Outline each uninfected red blood cell.
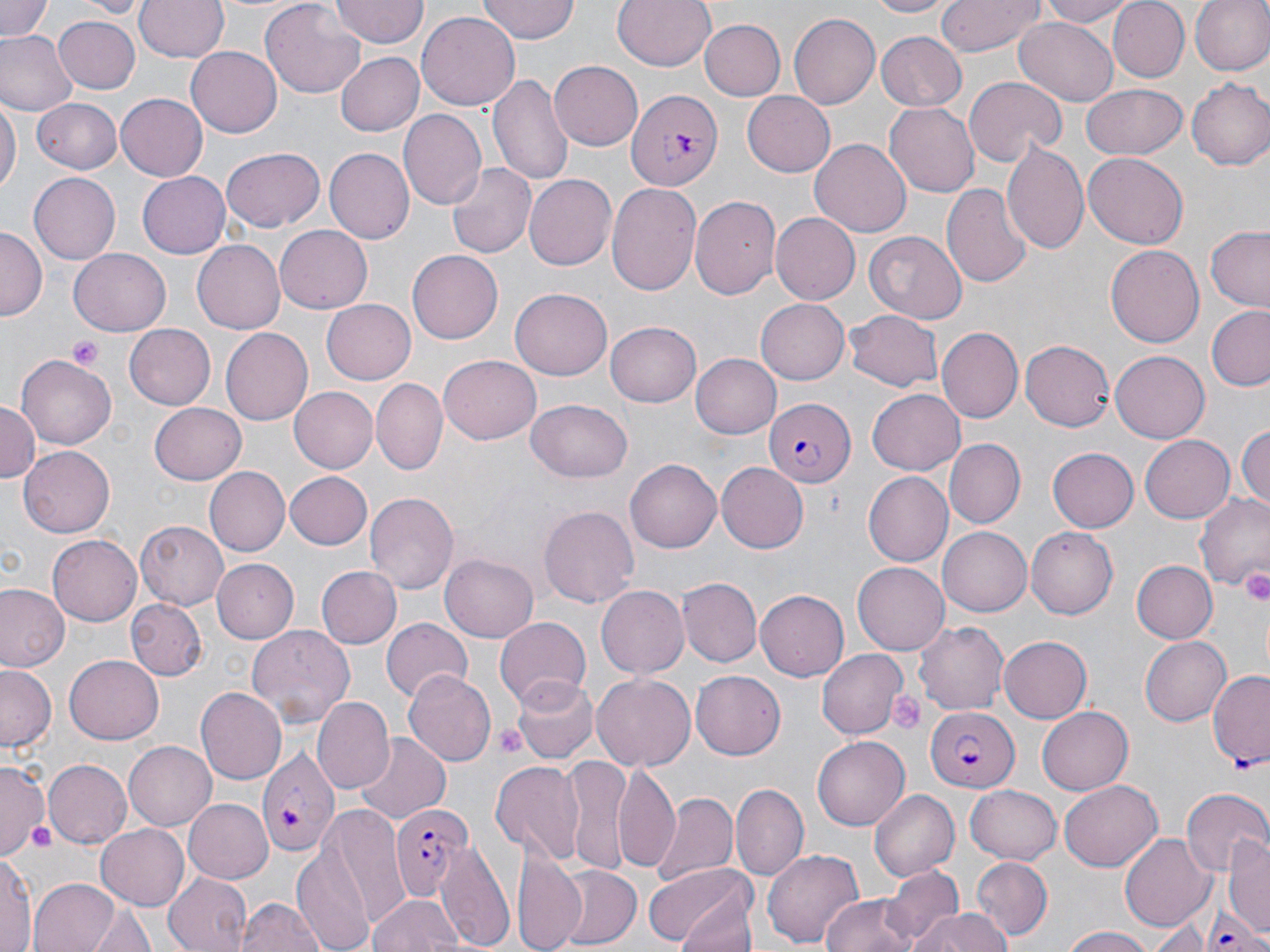
Approximate bounding boxes as (x1, y1, x2, y2) in pixels.
Uninfected red blood cells: (0, 0, 55, 42), (79, 0, 149, 18), (134, 0, 229, 63), (260, 0, 364, 96), (479, 0, 579, 42), (612, 0, 717, 71), (866, 0, 951, 18), (933, 0, 1045, 57), (1036, 0, 1138, 27), (1107, 0, 1190, 82), (1189, 0, 1270, 76), (331, 1, 430, 48), (416, 9, 519, 108), (787, 12, 879, 110), (53, 16, 140, 92), (700, 19, 786, 99), (1014, 19, 1119, 105), (873, 30, 967, 111), (0, 31, 75, 117), (185, 46, 280, 138), (334, 51, 425, 138), (548, 61, 643, 151), (488, 69, 574, 188), (963, 77, 1067, 166), (1186, 79, 1270, 171), (1082, 82, 1187, 159), (741, 90, 836, 175), (116, 93, 209, 181), (0, 95, 19, 200), (31, 99, 123, 173), (883, 101, 978, 197), (396, 108, 486, 207), (811, 139, 912, 238), (1002, 140, 1092, 255), (221, 148, 325, 233), (326, 148, 414, 243), (1084, 153, 1187, 249), (445, 162, 535, 259), (137, 171, 231, 259), (27, 173, 119, 264), (523, 173, 616, 272), (606, 182, 702, 294), (942, 183, 1032, 288), (690, 195, 781, 302), (770, 213, 860, 305), (276, 223, 373, 310), (1205, 226, 1270, 310), (0, 227, 45, 319), (864, 231, 967, 323), (192, 240, 286, 334), (1105, 243, 1204, 350), (69, 249, 170, 336), (405, 250, 502, 344), (511, 288, 613, 379), (322, 297, 416, 384), (755, 297, 848, 385), (1206, 307, 1270, 392), (844, 310, 945, 392), (606, 322, 701, 406), (125, 324, 215, 409), (219, 328, 312, 427), (934, 328, 1022, 424), (1021, 340, 1114, 431), (1111, 352, 1208, 441), (690, 353, 782, 439), (16, 354, 116, 450), (440, 355, 541, 445), (372, 378, 447, 474), (289, 388, 377, 471), (866, 390, 965, 474), (525, 398, 633, 482), (0, 401, 40, 486), (150, 403, 246, 485), (1236, 421, 1270, 512), (1141, 435, 1236, 522), (946, 439, 1025, 528), (19, 447, 115, 537), (1046, 448, 1137, 533), (626, 459, 721, 553), (717, 463, 809, 551), (203, 467, 289, 556), (864, 471, 953, 566), (286, 473, 371, 550), (1193, 490, 1269, 594), (364, 492, 460, 592), (539, 505, 640, 608), (134, 521, 227, 609), (938, 526, 1031, 617), (1026, 526, 1119, 619), (48, 534, 145, 625), (441, 554, 537, 641), (1131, 557, 1215, 644), (213, 559, 300, 643), (853, 561, 950, 655), (316, 565, 401, 650), (679, 577, 762, 666), (0, 583, 68, 672), (596, 585, 687, 678), (757, 589, 849, 680), (128, 598, 206, 679), (493, 616, 590, 713), (381, 618, 471, 704), (914, 619, 1009, 713), (247, 625, 356, 724), (997, 636, 1092, 723), (1138, 636, 1230, 725), (817, 648, 909, 739), (65, 656, 164, 743), (0, 665, 56, 752), (691, 669, 786, 757), (404, 671, 495, 768), (591, 673, 696, 773), (514, 677, 597, 763), (197, 688, 286, 782), (315, 697, 394, 792), (1037, 707, 1133, 794), (352, 733, 452, 824), (812, 736, 909, 831), (123, 741, 216, 830), (0, 758, 51, 855), (42, 758, 132, 850), (561, 758, 629, 871), (491, 760, 587, 864), (614, 763, 681, 877), (1057, 779, 1163, 872), (733, 784, 807, 877), (965, 785, 1063, 864), (1182, 789, 1270, 879), (868, 790, 959, 881), (653, 794, 737, 886), (183, 798, 273, 884), (315, 805, 410, 933), (96, 824, 192, 909), (1121, 833, 1214, 932), (1227, 835, 1270, 935), (297, 840, 375, 952), (432, 840, 516, 951), (516, 848, 587, 952), (764, 848, 864, 948), (1, 855, 38, 952), (971, 858, 1051, 942), (644, 863, 756, 949), (882, 863, 962, 943), (555, 866, 643, 949), (165, 869, 254, 952), (28, 877, 119, 952), (370, 894, 465, 952), (671, 895, 759, 952), (820, 895, 921, 952), (236, 897, 324, 952), (87, 903, 155, 952), (909, 909, 1015, 952), (1145, 910, 1223, 951), (1060, 925, 1156, 952).

Summary:
  - Plasmodium falciparum-infected red blood cell locations: (624, 88, 721, 194), (767, 397, 856, 488), (1207, 670, 1269, 770), (925, 706, 1019, 791), (255, 742, 336, 858), (393, 803, 471, 900), (1199, 899, 1269, 950)
  - Platelet locations: (66, 335, 106, 371), (1240, 571, 1270, 603), (889, 689, 925, 734), (494, 725, 526, 759), (22, 819, 62, 854)
  - Slide-level diagnosis: Plasmodium falciparum
  - Preparation: thin blood smear
  - Image size: 1270×952 pixels
  - Stain: May-Grünwald-Giemsa
  - Magnification: 1000x
  - Modality: light microscopy
  - Field of view: single